Point out each malaria parasite.
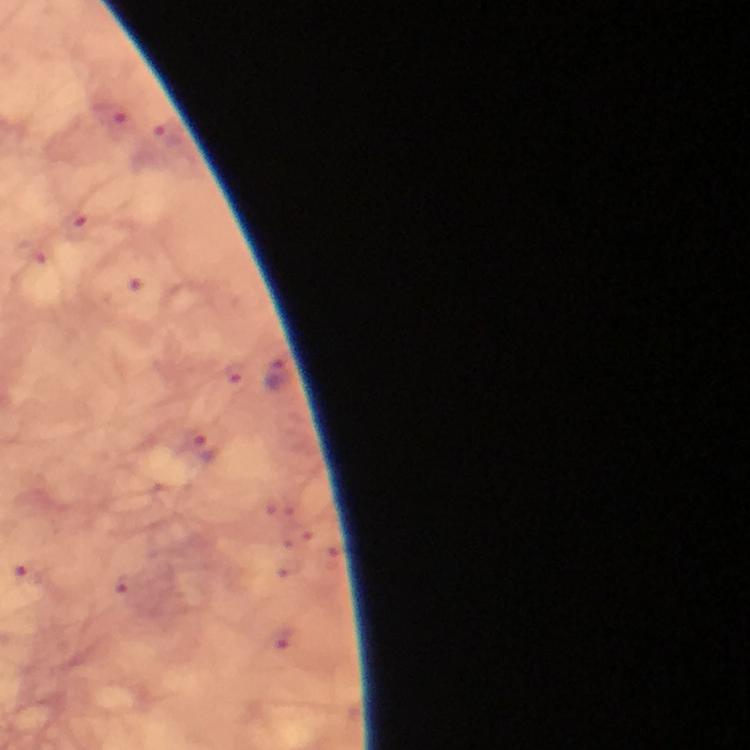

Approximate object centers, in pixels from the top-left corner.
Malaria parasites: (x=277, y=373), (x=207, y=448).

context = from a malaria diagnostic workup
immersion oil = applied
cropped from = a single field of view
capture = smartphone photograph through a microscope
magnification = 100x
image size = 750×750 pixels
stain = Giemsa
preparation = thick blood smear